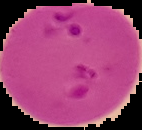
Cell region segmented out of the field of view; the surrounding area is masked to black. From a thin blood smear. Image is 142×130 pixels. Malaria status: parasitized.